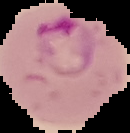

Malaria status: parasitized. Image is 130×133 pixels. The area outside the segmented cell region is set to black. From a thin blood smear.